Report the malaria status of this cell.
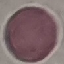
Uninfected.

Cell patch, automatically extracted from a larger field of view and resized to 64 × 64 pixels. Giemsa stain. Thin smear of blood. Acquired by smartphone through the microscope eyepiece.